Report the malaria status of this cell.
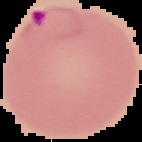
Parasitized.

preparation = thin blood film
image type = segmented cell region with the area outside set to black
image size = 142×142 pixels